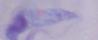

magnification = 1000x
identification = trypanosome
modality = micrograph